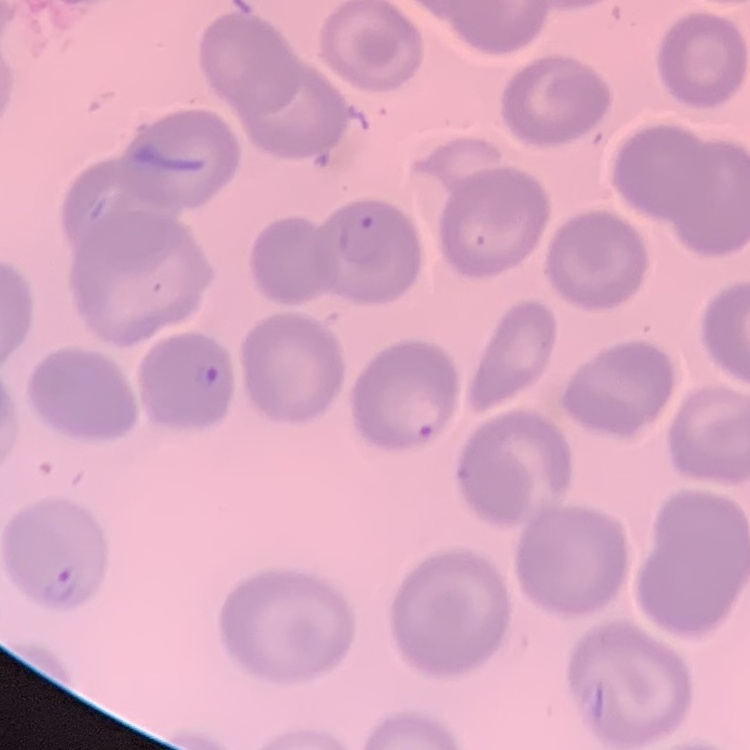 The erythrocytes show no rouleaux formation. Square crop of a larger photomicrograph. Field's or Giemsa stain. Thin peripheral smear.